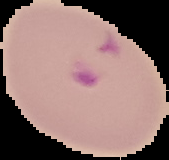

Summary:
  - Image type: cell region segmented out of the field of view; surrounding area masked to black
  - Preparation: thin blood smear
  - Image size: 169×160 pixels
  - Result: malaria parasites detected